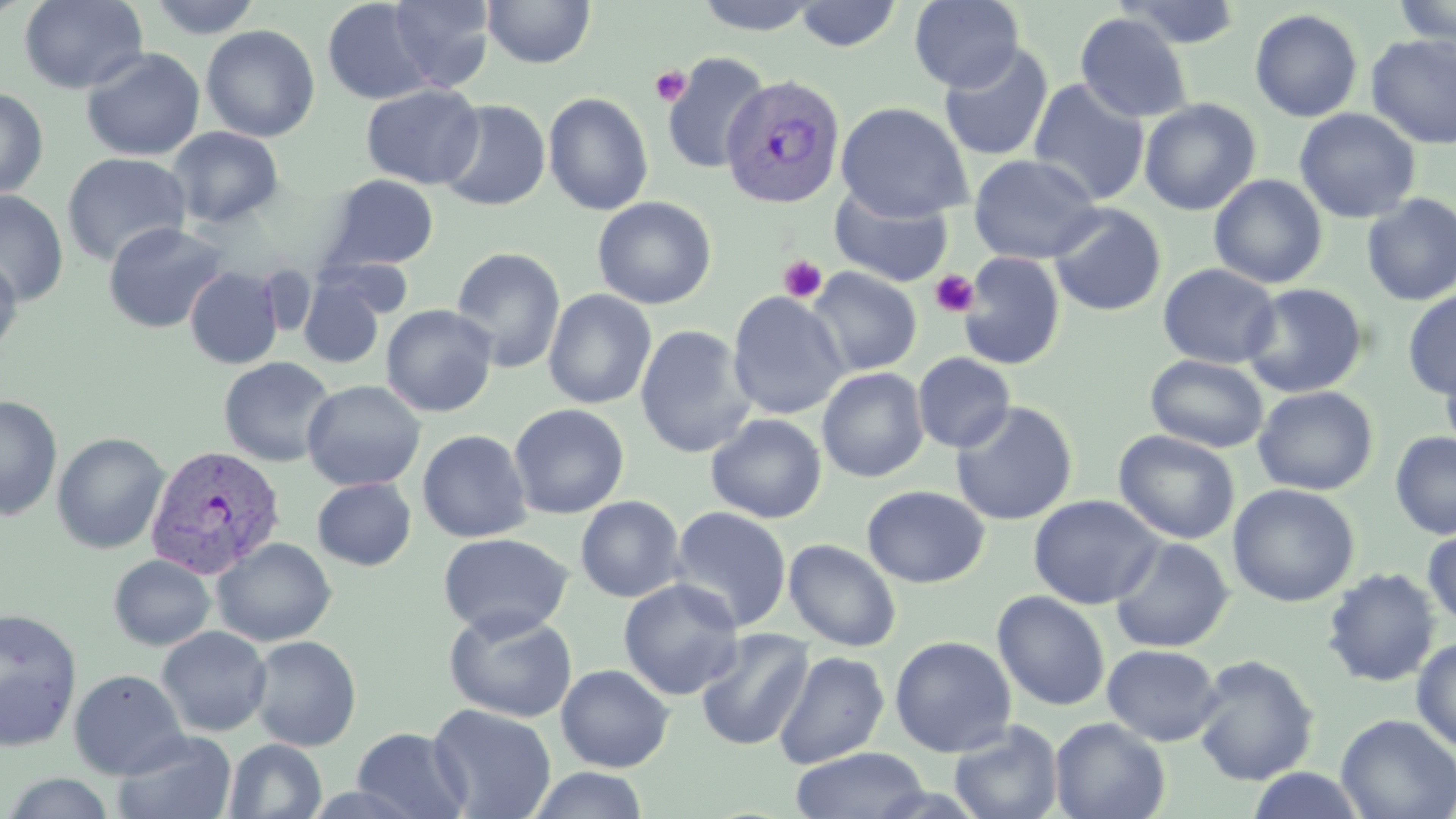
slide-level diagnosis = Plasmodium vivax
modality = optical microscopy
platelet locations = approximate bounding boxes as named x1/y1/x2/y2 corners in pixels: (x1=651, y1=64, x2=690, y2=107), (x1=778, y1=255, x2=827, y2=303), (x1=930, y1=269, x2=979, y2=317)
magnification = 1000x
stain = May-Grünwald-Giemsa
Plasmodium vivax-infected red blood cell locations = approximate bounding boxes as named x1/y1/x2/y2 corners in pixels: (x1=720, y1=74, x2=846, y2=209), (x1=144, y1=443, x2=286, y2=579)
image size = 1456×819 pixels
preparation = thin blood smear
field of view = single
uninfected red blood cell locations = approximate bounding boxes as named x1/y1/x2/y2 corners in pixels: (x1=18, y1=0, x2=148, y2=94), (x1=146, y1=0, x2=264, y2=39), (x1=321, y1=0, x2=436, y2=105), (x1=388, y1=0, x2=496, y2=91), (x1=482, y1=0, x2=596, y2=69), (x1=692, y1=0, x2=825, y2=35), (x1=909, y1=0, x2=1025, y2=92), (x1=1115, y1=0, x2=1244, y2=49), (x1=1393, y1=0, x2=1455, y2=50), (x1=793, y1=1, x2=903, y2=52), (x1=1250, y1=8, x2=1363, y2=122), (x1=1074, y1=13, x2=1193, y2=123), (x1=201, y1=25, x2=320, y2=142), (x1=1365, y1=34, x2=1456, y2=149), (x1=938, y1=42, x2=1054, y2=162), (x1=80, y1=47, x2=206, y2=161), (x1=662, y1=53, x2=770, y2=175), (x1=1028, y1=78, x2=1151, y2=205), (x1=361, y1=84, x2=484, y2=189), (x1=0, y1=86, x2=49, y2=199), (x1=544, y1=92, x2=653, y2=215), (x1=1139, y1=98, x2=1261, y2=216), (x1=437, y1=99, x2=550, y2=211), (x1=835, y1=102, x2=973, y2=220), (x1=1294, y1=108, x2=1421, y2=224), (x1=166, y1=126, x2=284, y2=229), (x1=61, y1=152, x2=191, y2=268), (x1=968, y1=153, x2=1102, y2=264), (x1=1209, y1=174, x2=1328, y2=289), (x1=324, y1=175, x2=439, y2=272), (x1=829, y1=185, x2=953, y2=287), (x1=0, y1=189, x2=69, y2=307), (x1=1360, y1=193, x2=1456, y2=306), (x1=592, y1=196, x2=717, y2=309), (x1=1048, y1=203, x2=1167, y2=317), (x1=102, y1=221, x2=229, y2=334), (x1=450, y1=247, x2=566, y2=373), (x1=957, y1=252, x2=1066, y2=370), (x1=0, y1=255, x2=23, y2=357), (x1=1157, y1=263, x2=1281, y2=368), (x1=255, y1=264, x2=316, y2=338), (x1=185, y1=266, x2=283, y2=370), (x1=806, y1=267, x2=922, y2=377), (x1=298, y1=275, x2=388, y2=369), (x1=1240, y1=282, x2=1370, y2=398), (x1=542, y1=289, x2=657, y2=409), (x1=1402, y1=290, x2=1456, y2=399), (x1=727, y1=291, x2=848, y2=420), (x1=380, y1=304, x2=498, y2=417), (x1=635, y1=324, x2=756, y2=459), (x1=1440, y1=346, x2=1456, y2=460), (x1=912, y1=353, x2=1016, y2=453), (x1=1145, y1=354, x2=1269, y2=452), (x1=219, y1=356, x2=337, y2=467), (x1=816, y1=367, x2=929, y2=483), (x1=301, y1=379, x2=426, y2=492), (x1=1252, y1=386, x2=1379, y2=496), (x1=0, y1=394, x2=63, y2=521), (x1=951, y1=401, x2=1078, y2=526), (x1=508, y1=403, x2=629, y2=519), (x1=706, y1=414, x2=827, y2=523), (x1=417, y1=429, x2=532, y2=543), (x1=1113, y1=429, x2=1241, y2=544), (x1=51, y1=432, x2=171, y2=554), (x1=1390, y1=432, x2=1456, y2=539), (x1=311, y1=477, x2=416, y2=570), (x1=1227, y1=483, x2=1361, y2=607), (x1=862, y1=485, x2=989, y2=588), (x1=1028, y1=494, x2=1162, y2=609), (x1=575, y1=495, x2=685, y2=603), (x1=669, y1=506, x2=792, y2=632), (x1=1422, y1=526, x2=1456, y2=630), (x1=438, y1=532, x2=573, y2=640), (x1=1108, y1=536, x2=1234, y2=653), (x1=211, y1=537, x2=337, y2=647), (x1=783, y1=539, x2=901, y2=652), (x1=108, y1=554, x2=216, y2=651), (x1=1321, y1=567, x2=1441, y2=687), (x1=618, y1=578, x2=744, y2=701), (x1=992, y1=589, x2=1110, y2=711), (x1=443, y1=607, x2=578, y2=723), (x1=0, y1=608, x2=82, y2=751), (x1=156, y1=626, x2=272, y2=737), (x1=694, y1=628, x2=814, y2=751), (x1=247, y1=635, x2=361, y2=752), (x1=889, y1=635, x2=1017, y2=757), (x1=1411, y1=636, x2=1456, y2=752), (x1=1102, y1=644, x2=1223, y2=746), (x1=773, y1=651, x2=889, y2=769), (x1=1191, y1=654, x2=1320, y2=786), (x1=556, y1=664, x2=674, y2=772), (x1=68, y1=668, x2=190, y2=780), (x1=427, y1=703, x2=557, y2=819), (x1=1336, y1=714, x2=1456, y2=819), (x1=1049, y1=717, x2=1170, y2=819), (x1=948, y1=719, x2=1064, y2=819), (x1=352, y1=727, x2=471, y2=818), (x1=111, y1=729, x2=238, y2=819), (x1=224, y1=739, x2=327, y2=819), (x1=790, y1=746, x2=930, y2=819), (x1=527, y1=767, x2=650, y2=819), (x1=1245, y1=767, x2=1368, y2=819), (x1=2, y1=773, x2=118, y2=818)